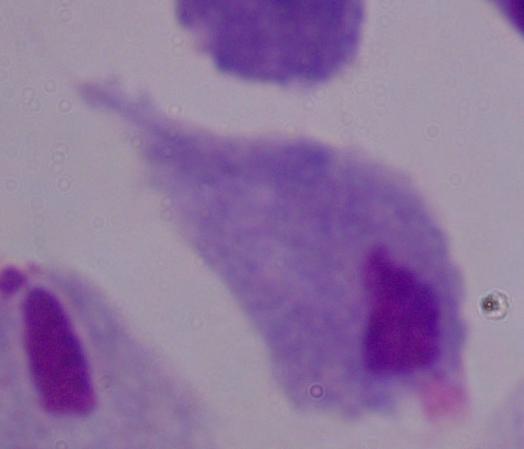

{
  "magnification": "1000x",
  "identification": "trichomonad",
  "modality": "micrograph"
}